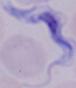 A trypanosome is shown. Micrograph. Captured at 1000x magnification.